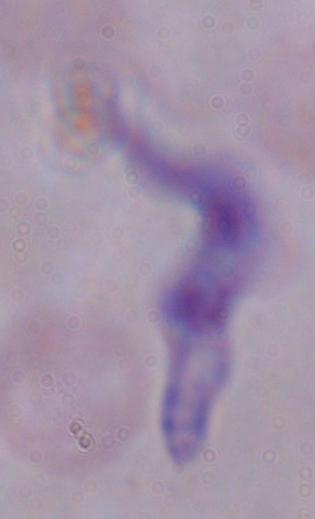 Captured at 1000x magnification. Photomicrograph. A trypanosome is shown.